Classify this cell by malaria status.
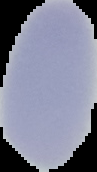
Uninfected.

Summary:
  - Image size: 97×172 pixels
  - Preparation: thin blood smear
  - Image type: segmented cell region on a black background